Classify this cell by malaria status.
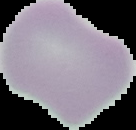
It is uninfected.

Cell region segmented out of the field of view; the surrounding area is masked to black. Image is 136×130 pixels. From a thin blood film.